Outline platelets.
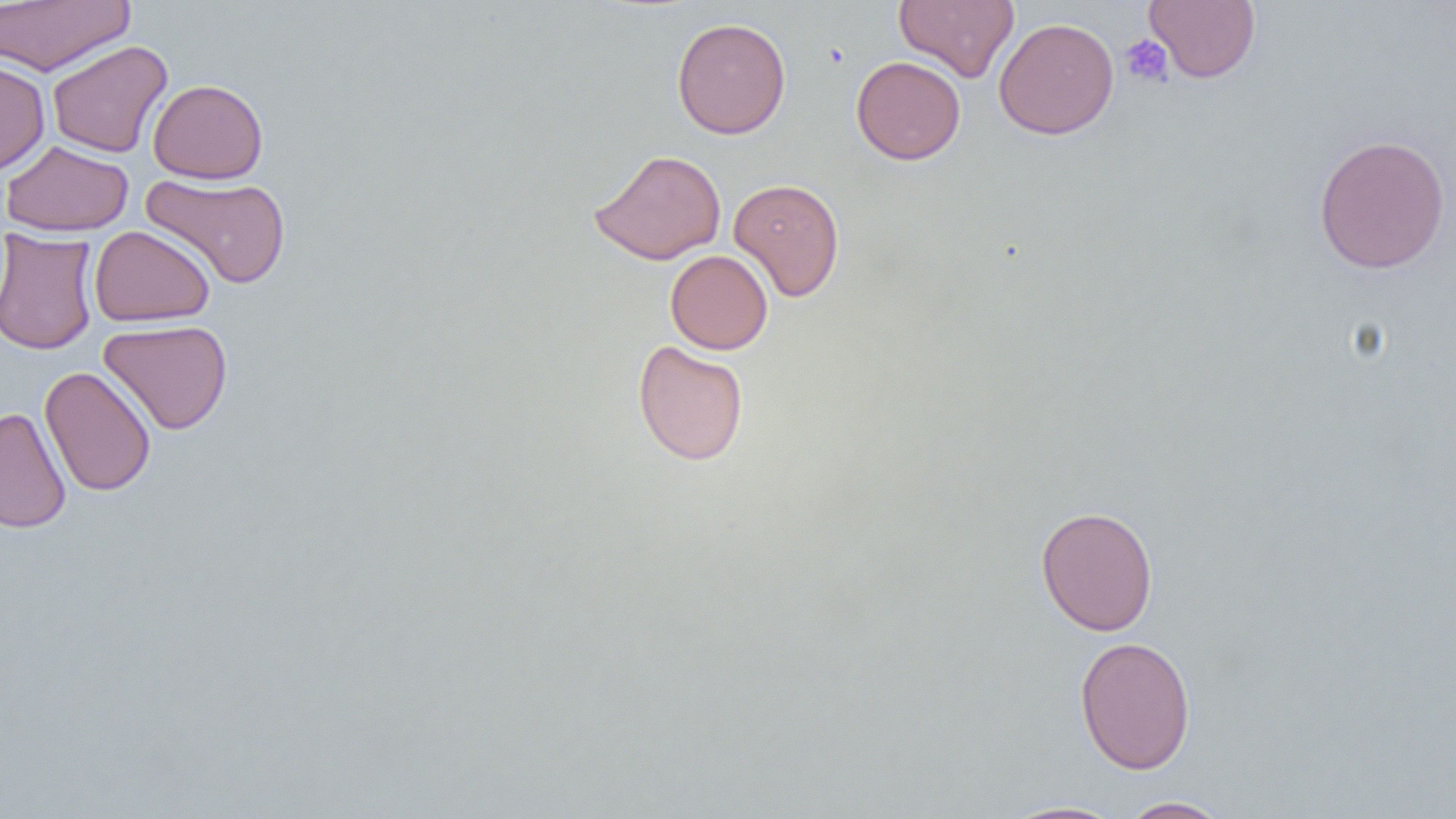

Approximate bounding boxes as (x1, y1, x2, y2) in pixels.
Platelets: (1120, 35, 1174, 88).

Uninfected red blood cell locations: (894, 0, 1019, 82), (1144, 0, 1261, 83), (1, 1, 134, 75), (672, 17, 791, 140), (993, 17, 1119, 140), (47, 40, 172, 158), (851, 55, 966, 165), (0, 59, 50, 176), (148, 78, 269, 184), (1313, 134, 1451, 275), (1, 140, 134, 237), (589, 149, 726, 265), (141, 172, 291, 290), (728, 177, 845, 301), (89, 225, 216, 326), (0, 229, 99, 355), (665, 250, 773, 354), (98, 320, 233, 435), (632, 340, 749, 466), (40, 365, 156, 497), (0, 407, 72, 533), (1035, 505, 1159, 636), (1074, 635, 1196, 774), (1117, 796, 1233, 818), (998, 800, 1128, 819). Slide-level diagnosis: negative for blood parasites. Image is 1456×819 pixels. Light microscopy. One field of a larger specimen. Captured at 1000x magnification. Thin blood film.